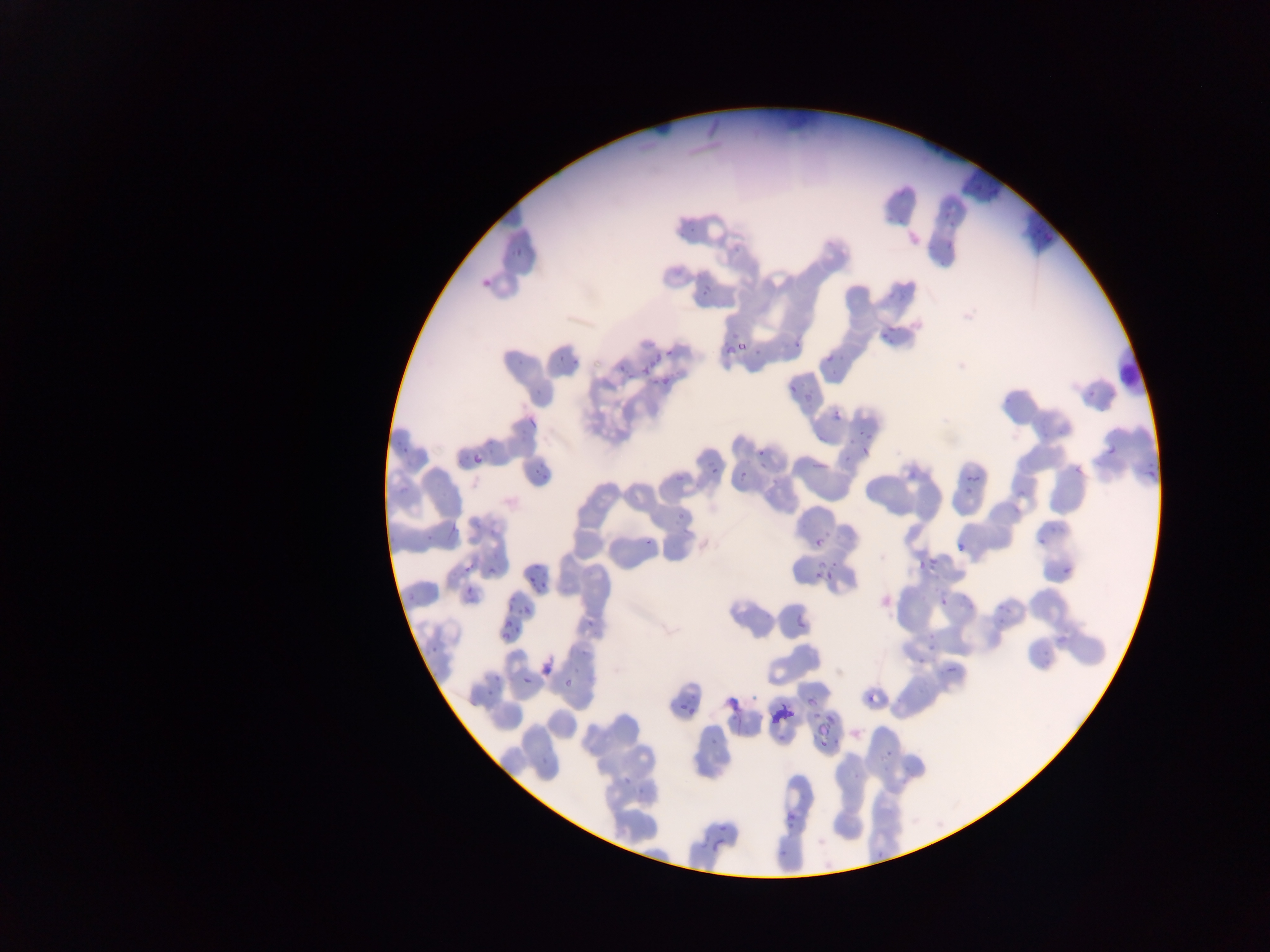 Approximate bounding boxes as left top right bottom in pixels. Leukocyte locations: 1120 347 1144 395. Malaria parasite locations: 514 247 522 257; 703 284 713 299; 738 342 745 352; 725 345 735 355; 655 347 661 362; 665 348 672 358; 827 355 835 364; 649 360 656 368; 643 368 651 376; 662 375 671 386; 787 384 797 392; 832 411 841 422; 528 416 538 427; 856 430 867 437; 1106 440 1119 456; 403 445 408 455; 860 447 869 455; 757 448 765 456; 468 455 480 466; 811 463 829 469; 712 466 720 475; 739 469 750 480; 539 471 549 480; 964 476 979 484; 814 537 824 546; 819 557 828 568; 466 562 477 574; 827 570 833 578; 818 571 824 579; 538 574 544 587; 466 586 474 594; 937 596 948 607; 521 603 532 617; 796 611 805 631; 505 617 514 632; 517 625 520 637; 502 631 510 639; 946 663 958 675; 522 677 535 684; 564 678 572 690; 870 692 887 706; 807 695 817 709; 680 703 690 710; 688 704 696 715; 819 720 830 737; 718 822 729 831; 698 835 709 851; 711 838 725 853 | approximate x y pixel centers of objects too small to bound: 531 579. Thin blood smear. Image is 1270×952 pixels. One field of view. Photographed through a microscope with a mobile-phone camera. Collected in Ghana.